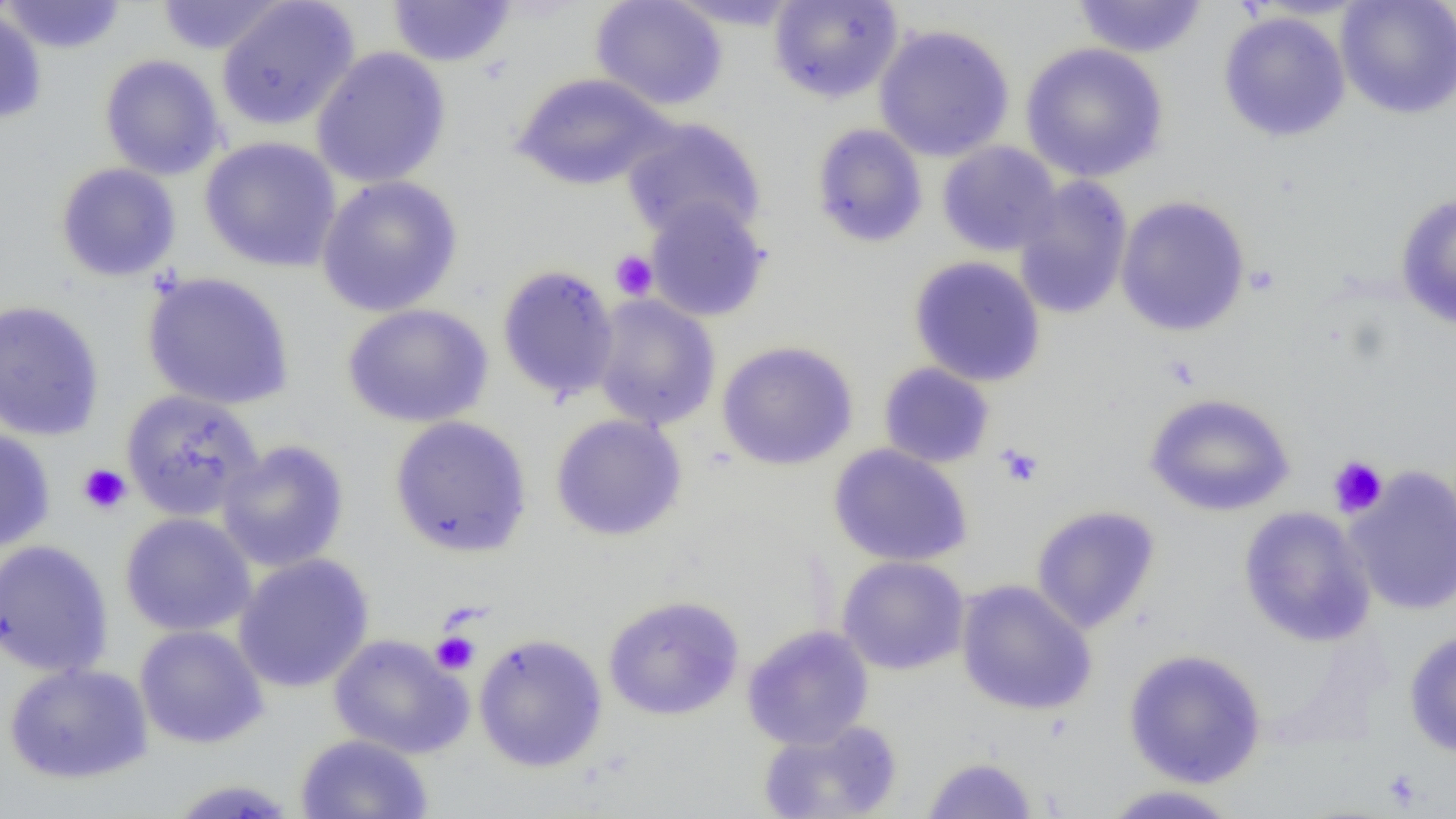
Approximate bounding boxes as (x1,y1)-(x2,y2) corner pairs in pixels. Platelet locations: (610,250)-(658,301), (996,443)-(1044,487), (1327,455)-(1388,518), (77,463)-(132,515), (430,630)-(480,675). Uninfected red blood cell locations: (0,0)-(128,55), (153,0)-(290,56), (215,0)-(360,132), (387,0)-(517,67), (590,0)-(729,111), (768,0)-(903,103), (1072,0)-(1209,58), (1335,0)-(1456,120), (664,1)-(807,31), (0,7)-(47,124), (1217,10)-(1351,142), (873,23)-(1015,162), (1020,42)-(1169,182), (310,47)-(451,188), (99,54)-(227,181), (510,72)-(674,190), (620,117)-(767,243), (811,123)-(928,248), (199,136)-(342,273), (937,141)-(1062,256), (55,162)-(181,282), (316,175)-(464,317), (1013,177)-(1133,320), (1394,191)-(1456,330), (1114,195)-(1251,337), (644,197)-(770,322), (908,255)-(1046,387), (496,264)-(620,404), (141,271)-(296,411), (590,295)-(721,430), (0,299)-(105,442), (341,303)-(494,428), (716,340)-(858,471), (877,362)-(995,469), (120,389)-(264,521), (1143,392)-(1296,517), (549,413)-(688,541), (389,415)-(532,558), (0,428)-(55,552), (216,440)-(350,573), (828,444)-(973,567), (1344,465)-(1456,617), (1030,505)-(1161,634), (1238,506)-(1376,647), (119,512)-(257,638), (0,539)-(114,678), (232,553)-(375,694), (837,555)-(970,675), (956,579)-(1098,716), (602,594)-(745,721), (134,624)-(269,749), (742,624)-(874,750), (1403,628)-(1456,758), (473,633)-(608,773), (328,634)-(473,759), (1123,648)-(1267,788), (2,661)-(154,784), (756,719)-(903,819), (294,733)-(433,819), (921,755)-(1039,818), (165,779)-(301,818), (1099,784)-(1244,818). Slide-level diagnosis: no evidence of blood parasites. Image is 1456×819 pixels. 1000x magnification. One field of a larger specimen. Light microscopy. Thin blood smear.